Describe the morphology of the erythrocytes.
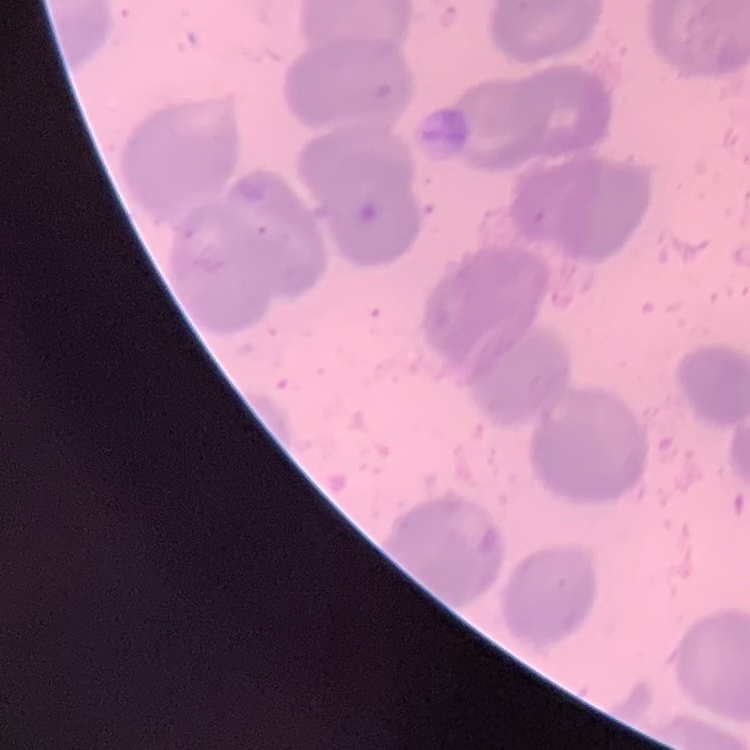

No rouleaux formation.

Summary:
  - Preparation: thin blood film
  - Stain: Field's or Giemsa
  - Image type: square crop of a larger photomicrograph